State which cell type is depicted.
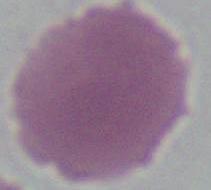
This is an erythrocyte.

Summary:
  - Modality: photomicrograph
  - Magnification: 1000x